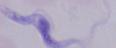

Micrograph. 1000x magnification. A trypanosome is seen.